Name the cell type shown.
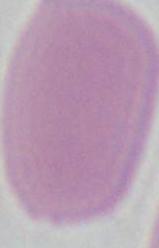

An erythrocyte.

Summary:
  - Magnification: 1000x
  - Modality: photomicrograph